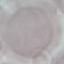
Malaria status: uninfected. Automatically extracted cell patch, resized to 64 × 64 pixels. Giemsa-stained preparation. Thin blood smear. Acquired by smartphone through the microscope eyepiece.